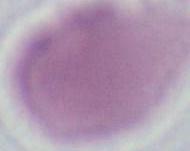

{
  "modality": "photomicrograph",
  "magnification": "1000x",
  "identification": "erythrocyte"
}